Report the malaria status of this cell.
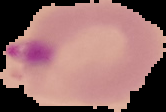

It is parasitized.

Summary:
  - Image size: 166×112 pixels
  - Preparation: thin blood film
  - Image type: segmented cell region with the area outside set to black